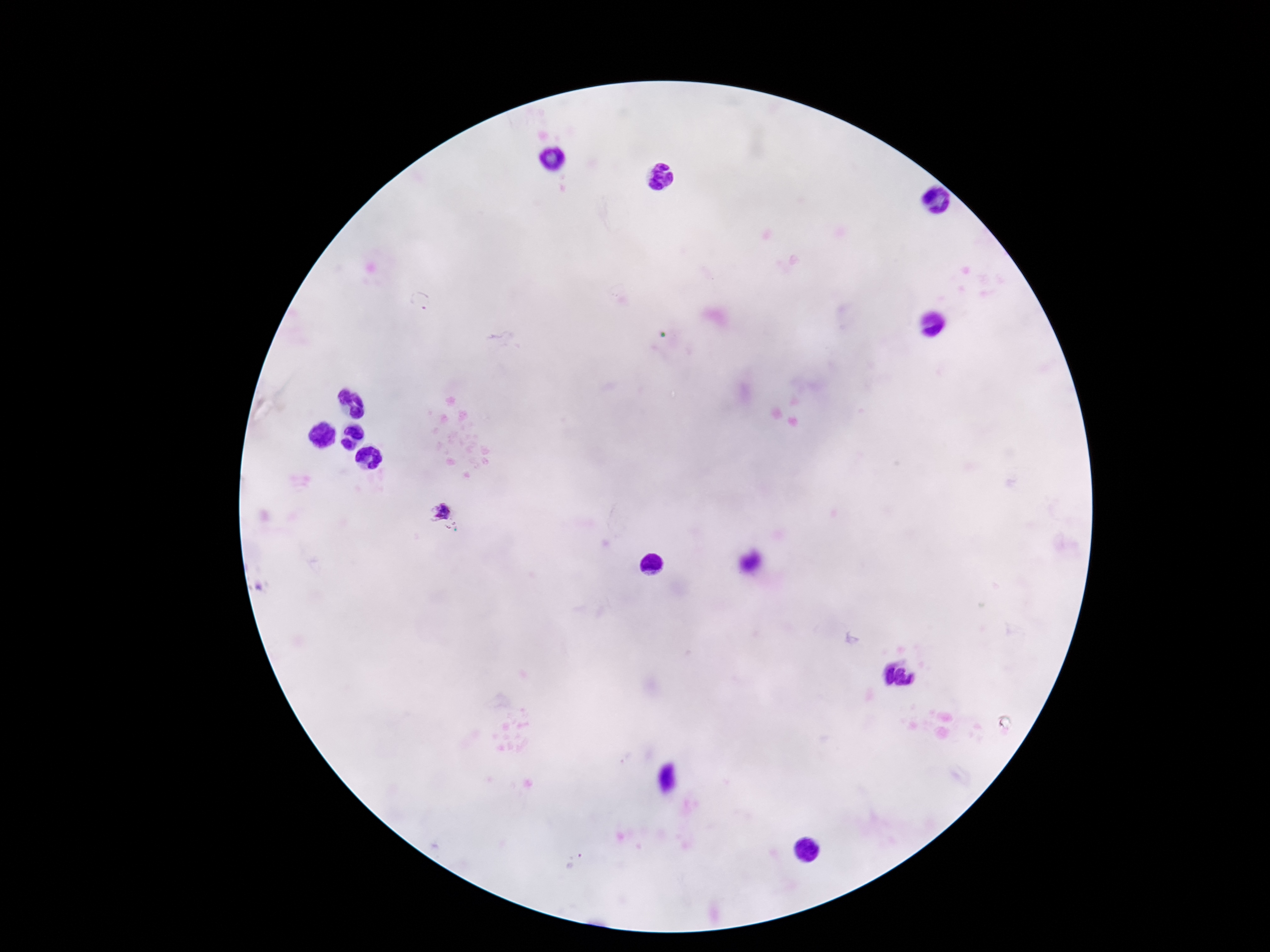

magnification = 100x
field of view = one from this slide
patient malaria status = infected
preparation = thick peripheral-blood smear
Plasmodium parasite locations = approximate centers as (x, y) in pixels: (421, 302), (441, 513)
image size = 1270×952 pixels
capture = smartphone camera through the microscope eyepiece
stain = Giemsa